Classify this cell by malaria status.
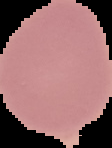
It is uninfected.

From a thin blood film. Image is 112×148 pixels. Cell region segmented out of the field of view; the surrounding area is masked to black.